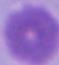

Summary:
  - Identification: red blood cell
  - Modality: photomicrograph
  - Magnification: 1000x